Classify this cell by malaria status.
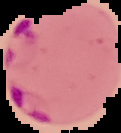
Parasitized.

{
  "image_type": "cell region segmented out of the field of view; surrounding area masked to black",
  "preparation": "thin blood film",
  "image_size": "121×133 pixels"
}